Name the blood parasite species.
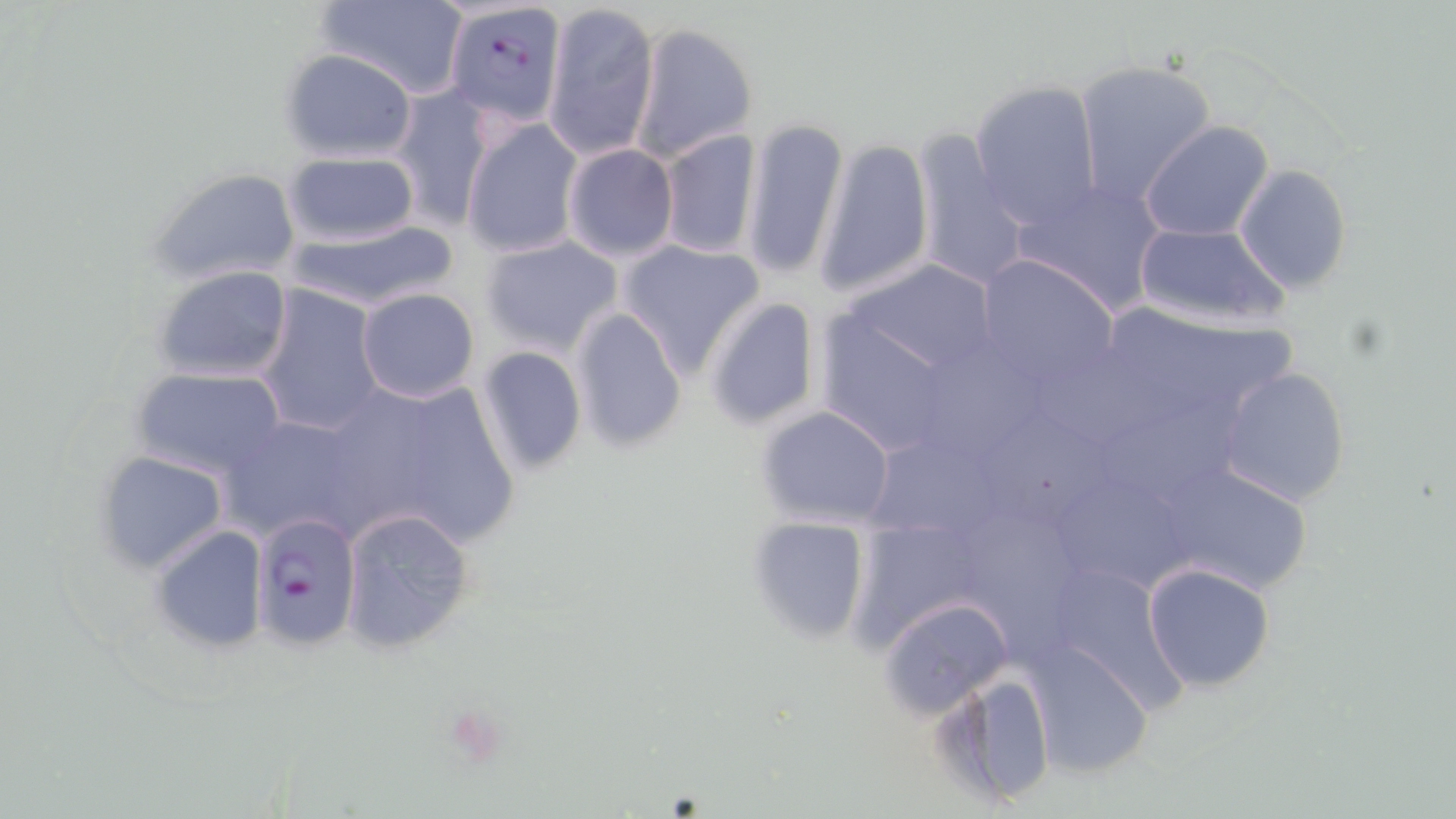

Plasmodium falciparum.

Summary:
  - Coordinate format: approximate bounding boxes as [x1, y1, x2, y2] in pixels
  - Uninfected red blood cell locations: [316, 0, 467, 100], [544, 1, 659, 161], [630, 21, 759, 161], [280, 48, 417, 160], [1073, 59, 1216, 207], [969, 79, 1104, 230], [390, 87, 494, 232], [739, 116, 848, 283], [461, 118, 584, 259], [1139, 121, 1276, 242], [659, 128, 761, 259], [910, 130, 1032, 291], [813, 137, 935, 299], [561, 144, 679, 263], [283, 150, 420, 247], [1234, 163, 1353, 294], [147, 167, 303, 287], [1015, 179, 1167, 314], [285, 219, 460, 313], [1132, 220, 1291, 331], [479, 236, 625, 357], [616, 239, 766, 377], [975, 255, 1119, 388], [840, 259, 1007, 383], [151, 265, 295, 382], [256, 285, 385, 438], [356, 289, 481, 404], [1110, 291, 1318, 394], [703, 296, 823, 431], [813, 297, 987, 458], [570, 308, 687, 451], [476, 346, 588, 475], [1032, 351, 1204, 452], [933, 359, 1039, 450], [1215, 365, 1353, 507], [131, 367, 285, 477], [326, 373, 520, 550], [1110, 390, 1255, 501], [754, 405, 897, 526], [219, 413, 366, 543], [987, 413, 1123, 521], [874, 430, 1005, 539], [95, 451, 230, 574], [1154, 460, 1316, 597], [1051, 462, 1196, 594], [338, 507, 476, 654], [972, 507, 1077, 645], [746, 515, 872, 645], [852, 520, 991, 642], [149, 525, 270, 651], [1040, 561, 1189, 712], [1140, 562, 1278, 692], [879, 596, 1015, 720], [1018, 639, 1153, 779], [940, 670, 1057, 809]
  - Plasmodium falciparum-infected red blood cell locations: [443, 0, 567, 129], [252, 512, 364, 651]
  - Preparation: thin blood film
  - Magnification: 1000x
  - Stain: May-Grünwald-Giemsa
  - Image size: 1456×819 pixels
  - Field of view: single
  - Modality: light microscopy